Assess for malaria.
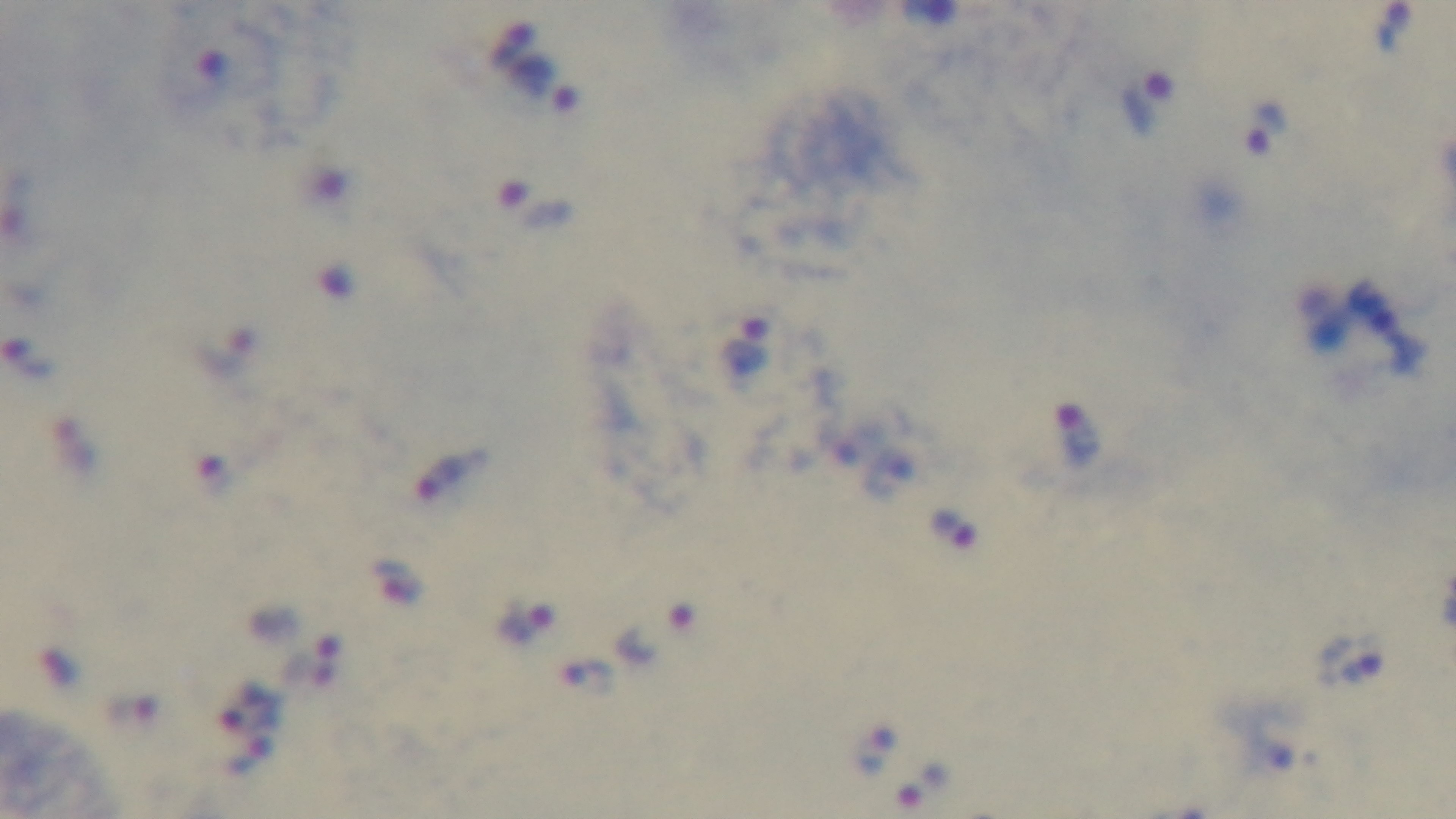

Positive.

stain = Giemsa
capture = mounted 4K digital camera
field of view = single
modality = light microscopy
objective = 100x oil immersion
preparation = thick